Report the malaria status of this cell.
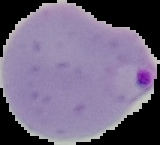

It is parasitized.

Cell region segmented out of the field of view; the surrounding area is masked to black. From a thin blood smear. Image is 160×145 pixels.